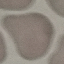
malaria_status: uninfected
capture: smartphone camera at the microscope eyepiece
preparation: thin smear
image_type: cell patch, automatically extracted from a larger field of view and resized to 64 × 64 pixels
stain: Giemsa